Locate and identify every blood parasite.
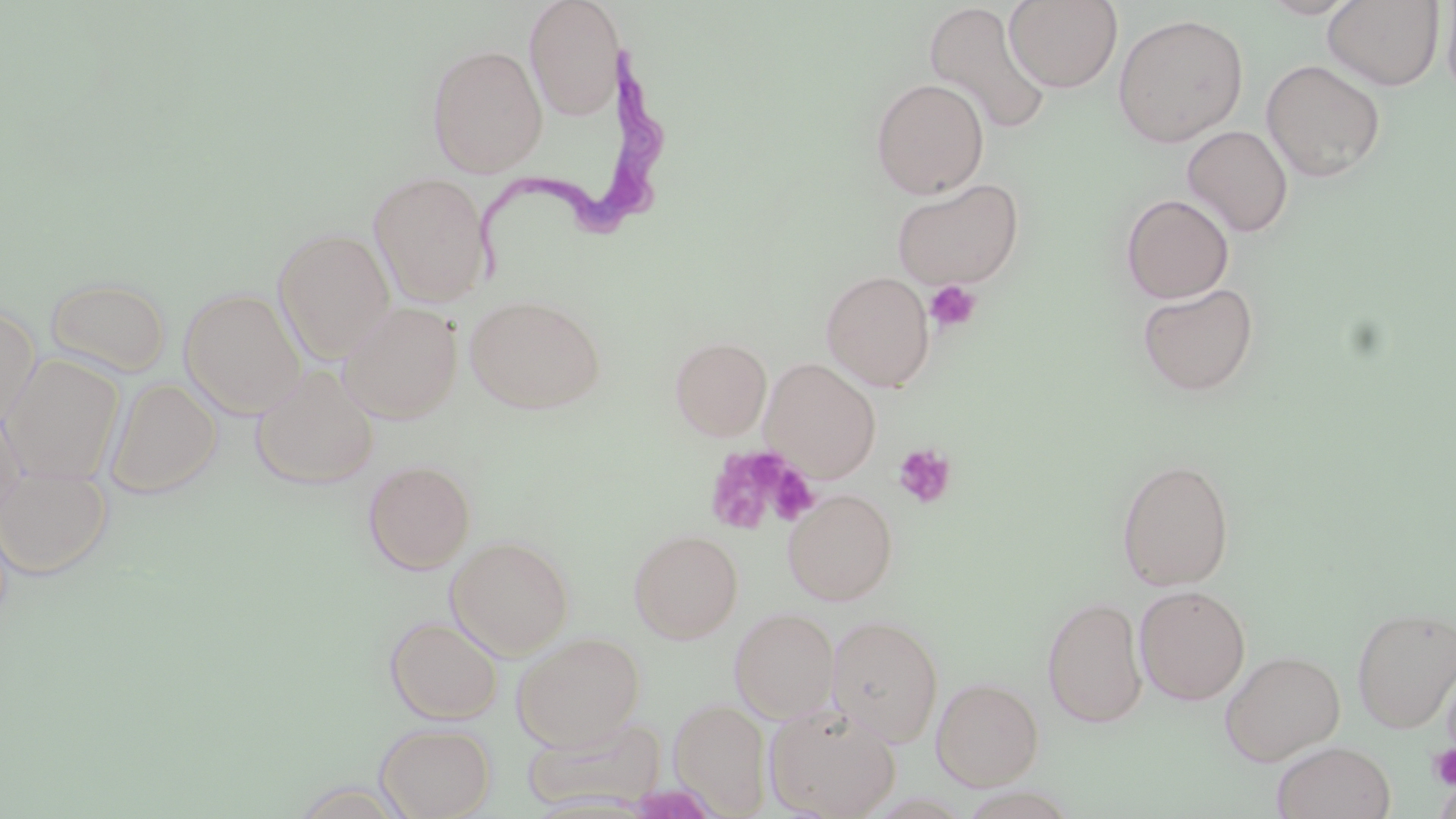
Approximate bounding boxes as named x1/y1/x2/y2 corners in pixels.
Trypanosoma brucei: (x1=479, y1=42, x2=674, y2=289).
No Plasmodium falciparum, Plasmodium ovale, Plasmodium malariae, Plasmodium vivax, or Babesia divergens observed.

Uninfected red blood cell locations: (x1=523, y1=0, x2=626, y2=121), (x1=1004, y1=0, x2=1123, y2=92), (x1=1258, y1=0, x2=1362, y2=19), (x1=922, y1=1, x2=1052, y2=137), (x1=1322, y1=1, x2=1446, y2=91), (x1=1441, y1=2, x2=1456, y2=106), (x1=1112, y1=13, x2=1249, y2=147), (x1=427, y1=44, x2=547, y2=178), (x1=1261, y1=59, x2=1386, y2=183), (x1=870, y1=78, x2=989, y2=198), (x1=1181, y1=125, x2=1293, y2=238), (x1=368, y1=171, x2=493, y2=308), (x1=890, y1=178, x2=1025, y2=289), (x1=1120, y1=193, x2=1234, y2=304), (x1=273, y1=228, x2=395, y2=363), (x1=821, y1=270, x2=935, y2=391), (x1=47, y1=276, x2=170, y2=377), (x1=1136, y1=282, x2=1260, y2=397), (x1=179, y1=287, x2=306, y2=418), (x1=465, y1=294, x2=605, y2=414), (x1=338, y1=301, x2=463, y2=424), (x1=0, y1=307, x2=39, y2=430), (x1=669, y1=337, x2=772, y2=441), (x1=3, y1=354, x2=124, y2=485), (x1=760, y1=358, x2=881, y2=483), (x1=251, y1=365, x2=380, y2=490), (x1=105, y1=377, x2=221, y2=499), (x1=0, y1=402, x2=28, y2=524), (x1=1116, y1=458, x2=1235, y2=591), (x1=362, y1=459, x2=476, y2=574), (x1=0, y1=464, x2=112, y2=578), (x1=783, y1=488, x2=898, y2=606), (x1=629, y1=529, x2=743, y2=644), (x1=446, y1=535, x2=574, y2=659), (x1=1134, y1=585, x2=1250, y2=706), (x1=1041, y1=596, x2=1148, y2=729), (x1=1351, y1=605, x2=1456, y2=733), (x1=729, y1=607, x2=839, y2=723), (x1=826, y1=614, x2=944, y2=747), (x1=385, y1=616, x2=502, y2=724), (x1=512, y1=632, x2=645, y2=750), (x1=1220, y1=650, x2=1345, y2=766), (x1=932, y1=676, x2=1044, y2=790), (x1=670, y1=699, x2=772, y2=816), (x1=764, y1=703, x2=901, y2=819), (x1=521, y1=715, x2=667, y2=813), (x1=375, y1=723, x2=495, y2=819), (x1=1271, y1=740, x2=1396, y2=819). Platelet locations: (x1=925, y1=280, x2=982, y2=332), (x1=892, y1=443, x2=957, y2=508), (x1=705, y1=448, x2=793, y2=534), (x1=765, y1=463, x2=819, y2=524), (x1=1428, y1=744, x2=1456, y2=790). Slide-level diagnosis: Trypanosoma brucei. 1000x magnification. Image is 1456×819 pixels. Single field of view. May-Grünwald-Giemsa-stained preparation. Optical microscopy. Thin blood smear.